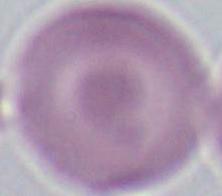 1000x magnification. Micrograph. An erythrocyte is shown.